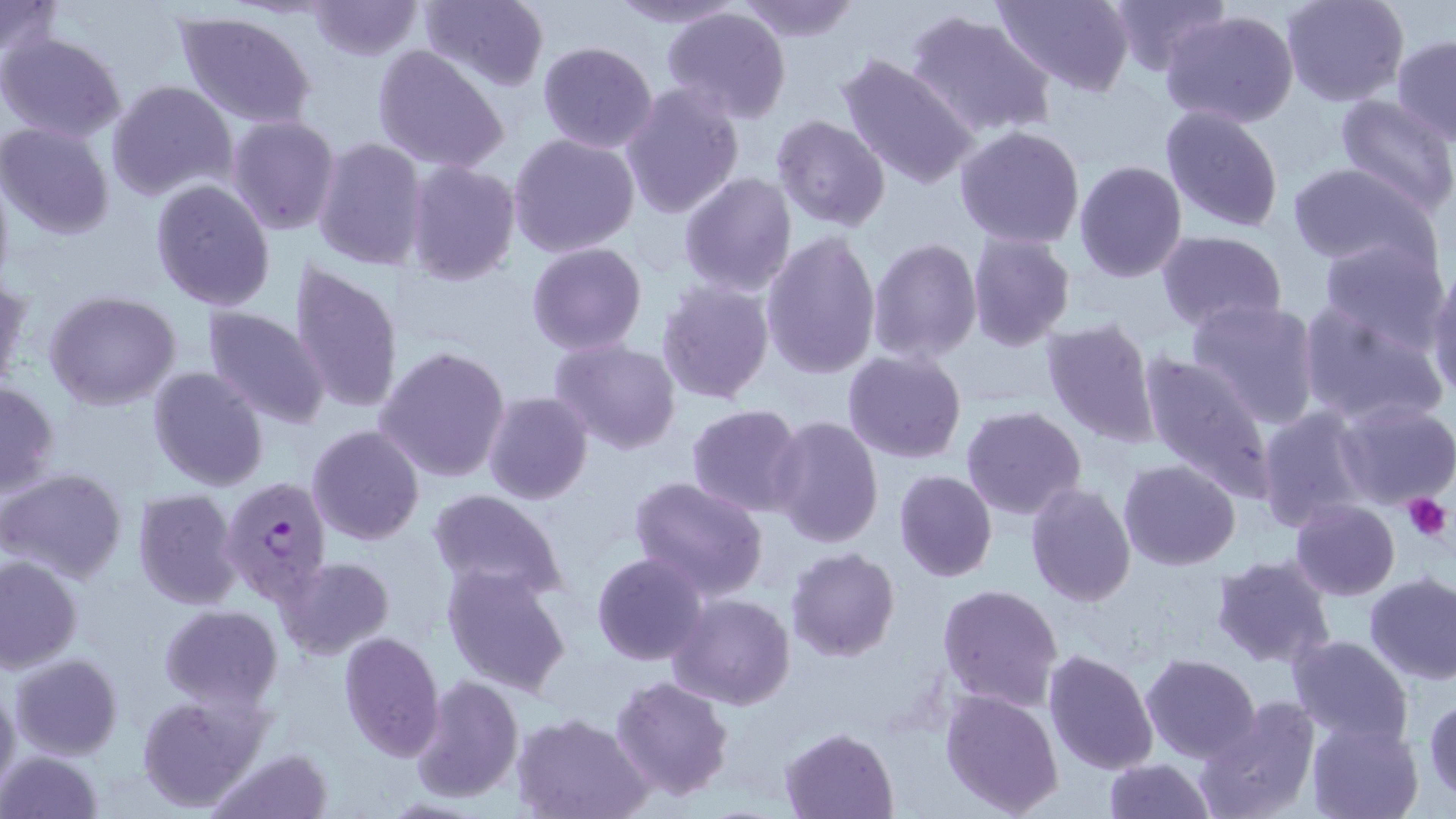 Approximate bounding boxes as named x1/y1/x2/y2 corners in pixels. Plasmodium falciparum-infected red blood cell locations: (x1=223, y1=475, x2=336, y2=606). Uninfected red blood cell locations: (x1=0, y1=0, x2=62, y2=61), (x1=306, y1=0, x2=425, y2=60), (x1=416, y1=0, x2=550, y2=91), (x1=604, y1=0, x2=747, y2=28), (x1=731, y1=0, x2=863, y2=42), (x1=993, y1=0, x2=1138, y2=96), (x1=1105, y1=0, x2=1231, y2=75), (x1=1280, y1=0, x2=1408, y2=108), (x1=661, y1=6, x2=793, y2=124), (x1=904, y1=7, x2=1058, y2=142), (x1=173, y1=9, x2=318, y2=130), (x1=1159, y1=9, x2=1301, y2=129), (x1=1, y1=33, x2=127, y2=144), (x1=1392, y1=35, x2=1456, y2=143), (x1=536, y1=40, x2=659, y2=153), (x1=371, y1=44, x2=511, y2=173), (x1=837, y1=52, x2=980, y2=191), (x1=585, y1=61, x2=718, y2=191), (x1=106, y1=80, x2=238, y2=203), (x1=620, y1=83, x2=745, y2=220), (x1=1333, y1=93, x2=1456, y2=217), (x1=1160, y1=105, x2=1285, y2=234), (x1=226, y1=115, x2=342, y2=237), (x1=770, y1=115, x2=891, y2=233), (x1=1, y1=122, x2=117, y2=240), (x1=953, y1=124, x2=1087, y2=248), (x1=507, y1=133, x2=641, y2=259), (x1=313, y1=137, x2=427, y2=271), (x1=1074, y1=159, x2=1188, y2=283), (x1=404, y1=161, x2=521, y2=285), (x1=1287, y1=162, x2=1438, y2=267), (x1=0, y1=168, x2=15, y2=294), (x1=678, y1=171, x2=797, y2=297), (x1=149, y1=178, x2=277, y2=311), (x1=1156, y1=230, x2=1287, y2=332), (x1=760, y1=231, x2=882, y2=379), (x1=967, y1=231, x2=1076, y2=351), (x1=1318, y1=237, x2=1446, y2=344), (x1=867, y1=238, x2=982, y2=363), (x1=526, y1=242, x2=647, y2=354), (x1=287, y1=259, x2=405, y2=416), (x1=1425, y1=262, x2=1456, y2=403), (x1=0, y1=273, x2=28, y2=395), (x1=656, y1=281, x2=774, y2=404), (x1=44, y1=291, x2=183, y2=410), (x1=1185, y1=298, x2=1322, y2=430), (x1=1298, y1=301, x2=1450, y2=428), (x1=201, y1=306, x2=332, y2=429), (x1=1041, y1=318, x2=1163, y2=446), (x1=549, y1=338, x2=681, y2=456), (x1=375, y1=346, x2=511, y2=484), (x1=1137, y1=347, x2=1278, y2=505), (x1=842, y1=350, x2=966, y2=463), (x1=148, y1=366, x2=269, y2=494), (x1=0, y1=380, x2=59, y2=499), (x1=481, y1=391, x2=594, y2=507), (x1=1333, y1=398, x2=1455, y2=510), (x1=1256, y1=403, x2=1371, y2=532), (x1=686, y1=404, x2=807, y2=518), (x1=658, y1=405, x2=794, y2=598), (x1=961, y1=406, x2=1087, y2=521), (x1=768, y1=415, x2=884, y2=550), (x1=306, y1=425, x2=426, y2=546), (x1=1118, y1=459, x2=1240, y2=570), (x1=2, y1=467, x2=129, y2=585), (x1=893, y1=469, x2=997, y2=582), (x1=628, y1=477, x2=770, y2=603), (x1=1024, y1=482, x2=1136, y2=607), (x1=132, y1=488, x2=243, y2=609), (x1=429, y1=489, x2=569, y2=603), (x1=1289, y1=500, x2=1399, y2=600), (x1=786, y1=547, x2=900, y2=663), (x1=592, y1=551, x2=708, y2=665), (x1=0, y1=554, x2=84, y2=673), (x1=275, y1=555, x2=396, y2=660), (x1=1211, y1=555, x2=1336, y2=669), (x1=441, y1=564, x2=572, y2=697), (x1=1364, y1=574, x2=1456, y2=685), (x1=938, y1=582, x2=1063, y2=711), (x1=668, y1=593, x2=795, y2=711), (x1=160, y1=605, x2=283, y2=709), (x1=337, y1=631, x2=444, y2=760), (x1=1287, y1=634, x2=1414, y2=746), (x1=1042, y1=648, x2=1159, y2=776), (x1=11, y1=653, x2=124, y2=759), (x1=1140, y1=653, x2=1261, y2=763), (x1=409, y1=674, x2=523, y2=805), (x1=612, y1=674, x2=735, y2=802), (x1=0, y1=678, x2=20, y2=799), (x1=940, y1=688, x2=1064, y2=817), (x1=135, y1=692, x2=268, y2=811), (x1=1425, y1=693, x2=1456, y2=802), (x1=1195, y1=698, x2=1321, y2=819), (x1=511, y1=712, x2=651, y2=819), (x1=1306, y1=719, x2=1423, y2=819), (x1=781, y1=728, x2=897, y2=818), (x1=209, y1=747, x2=332, y2=819), (x1=1, y1=749, x2=106, y2=819), (x1=1103, y1=757, x2=1216, y2=818). Platelet locations: (x1=1402, y1=491, x2=1450, y2=542). Slide-level diagnosis: Plasmodium falciparum. 1000x magnification. Image is 1456×819 pixels. Single field of view. Light microscopy. May-Grünwald-Giemsa stain. Thin blood film.